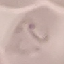

Result: malaria parasites detected. Photographed with a smartphone camera at the microscope eyepiece. Giemsa-stained preparation. Automatically extracted cell patch, resized to 64 × 64 pixels. Thin blood film.